State which cell type is depicted.
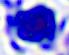
A leukocyte.

magnification = 400x
modality = photomicrograph